Locate and identify every blood parasite.
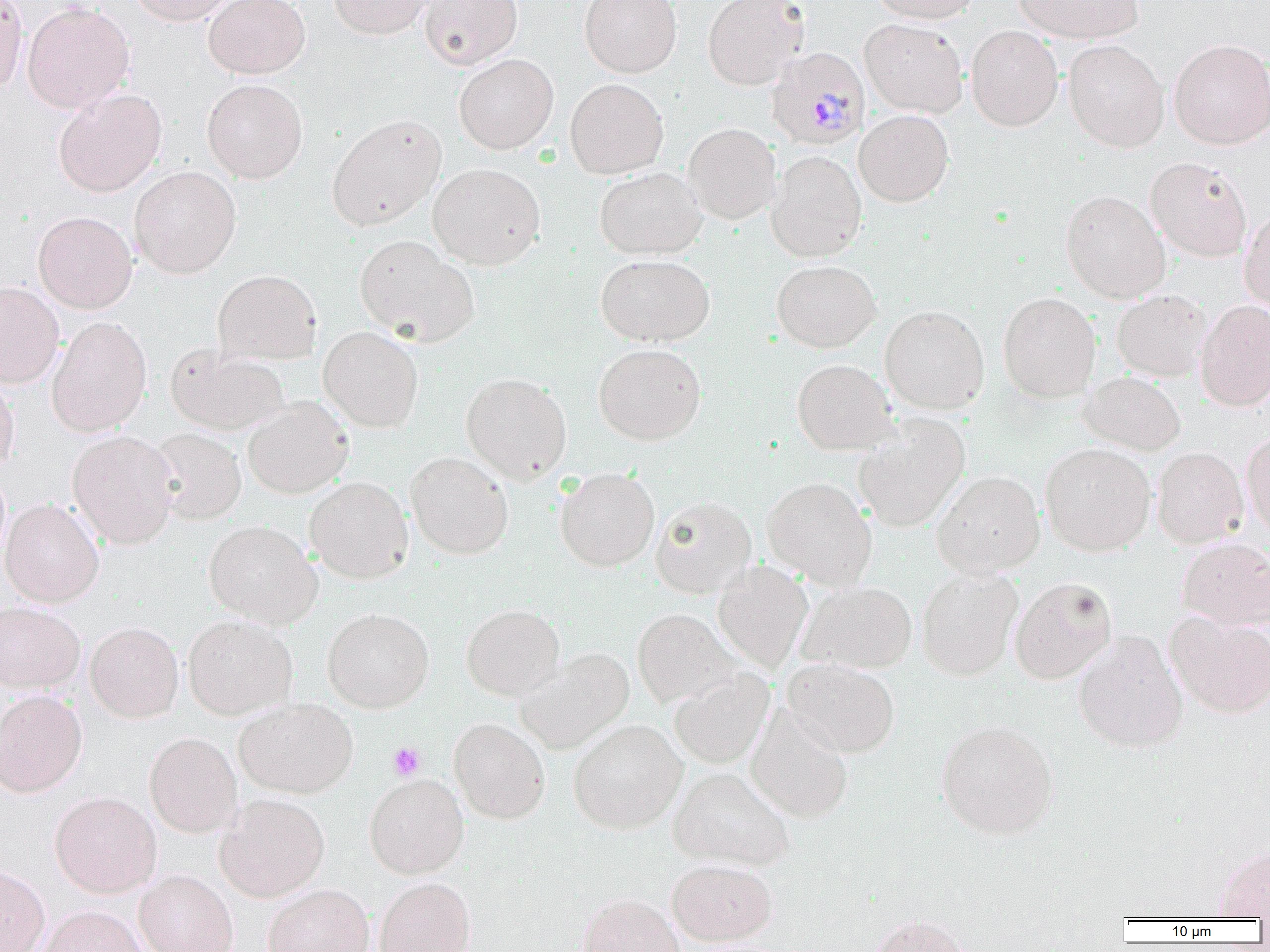
Approximate bounding boxes as (x1,y1)-(x2,y2) corner pairs in pixels.
Plasmodium malariae-infected red blood cells: (766,47)-(870,150).
No Plasmodium falciparum, Plasmodium ovale, Plasmodium vivax, Babesia divergens, or Trypanosoma brucei observed.

Platelet locations: (388,742)-(426,781). Uninfected red blood cell locations: (0,0)-(28,92), (128,0)-(238,25), (204,0)-(310,79), (330,0)-(433,39), (419,0)-(522,69), (579,0)-(682,78), (702,0)-(808,90), (870,0)-(981,23), (1014,0)-(1143,43), (22,2)-(135,113), (859,18)-(969,118), (966,25)-(1063,131), (1168,38)-(1270,149), (1063,39)-(1170,152), (453,53)-(558,154), (202,78)-(308,184), (565,78)-(668,179), (53,88)-(167,197), (854,110)-(954,206), (327,113)-(447,230), (683,123)-(781,224), (766,150)-(867,262), (1145,157)-(1252,261), (427,162)-(545,269), (129,166)-(241,278), (594,166)-(707,259), (1060,190)-(1171,303), (1239,209)-(1270,315), (33,211)-(137,313), (354,235)-(480,347), (595,254)-(715,346), (771,260)-(880,352), (212,269)-(322,365), (0,282)-(63,387), (1112,290)-(1211,381), (998,292)-(1101,401), (1196,299)-(1270,412), (879,305)-(990,414), (47,316)-(152,437), (318,326)-(423,432), (593,343)-(706,445), (165,344)-(290,436), (792,359)-(898,454), (1080,371)-(1186,456), (460,372)-(572,484), (0,377)-(19,478), (242,397)-(353,498), (854,413)-(970,532), (149,428)-(247,525), (67,430)-(179,548), (1241,431)-(1270,538), (1040,442)-(1156,556), (1152,446)-(1249,548), (405,451)-(513,559), (555,467)-(659,571), (932,470)-(1045,577), (305,476)-(414,584), (762,477)-(877,589), (650,496)-(756,598), (1,498)-(104,607), (203,520)-(322,628), (1178,538)-(1270,630), (713,561)-(813,674), (916,567)-(1023,681), (1009,576)-(1118,684), (796,580)-(917,674), (0,601)-(85,693), (461,604)-(564,701), (322,607)-(434,713), (632,609)-(743,708), (1166,612)-(1270,718), (183,614)-(297,719), (85,621)-(184,723), (1073,631)-(1188,753), (515,649)-(633,754), (782,658)-(900,757), (669,667)-(775,769), (0,689)-(88,797), (234,699)-(358,798), (746,705)-(853,823), (449,717)-(550,823), (568,719)-(687,834), (936,719)-(1058,839), (144,731)-(242,837), (668,766)-(795,871), (364,773)-(469,877), (50,791)-(162,897), (214,793)-(329,902), (1212,844)-(1270,918), (666,858)-(778,946), (0,865)-(50,952), (134,869)-(238,952), (374,877)-(476,952), (262,884)-(374,952), (577,893)-(685,952), (36,905)-(148,952), (865,915)-(975,952). Slide-level diagnosis: Plasmodium malariae. Thin blood smear. Light microscopy. One field of a larger specimen. Captured at 1000x magnification. Image is 1270×952 pixels.